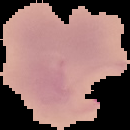
Summary:
  - Image size: 130×130 pixels
  - Malaria status: parasitized
  - Image type: segmented cell region with the area outside set to black
  - Preparation: thin blood smear